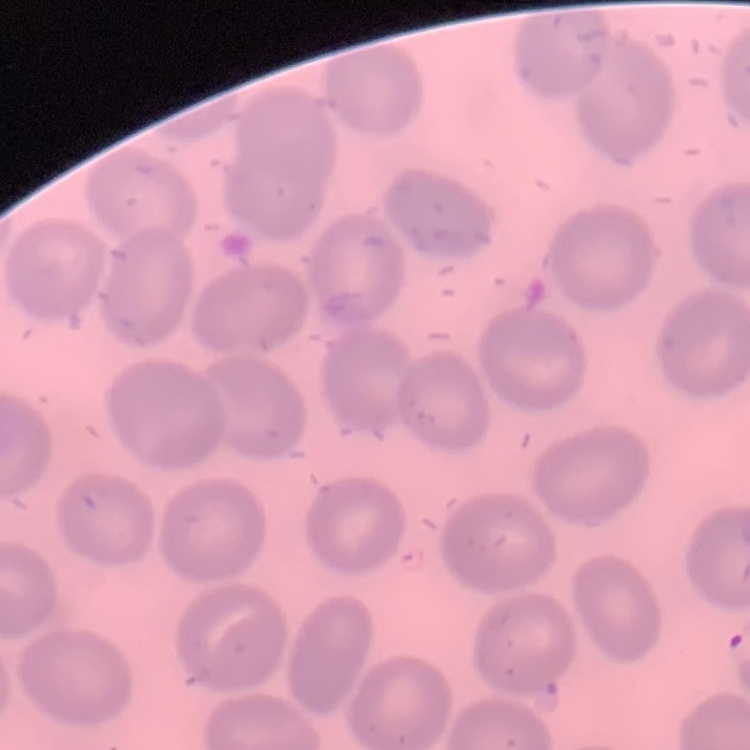

Summary:
  - Erythrocyte morphology: no rouleaux formation
  - Image type: one tile cut from a larger photomicrograph
  - Preparation: thin blood smear
  - Stain: Field's or Giemsa